Identify the parasite.
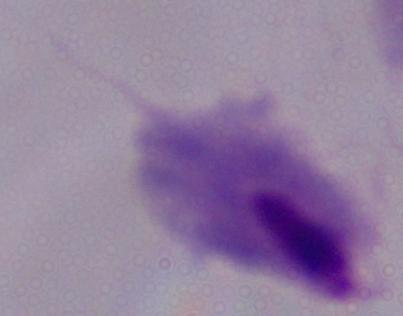
A trichomonad.

modality: micrograph
magnification: 1000x